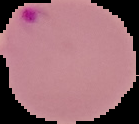 Result: Plasmodium parasites detected. Cell region segmented out of the field of view; the surrounding area is masked to black. Image is 139×124 pixels. From a thin blood film.